Report the malaria status of this cell.
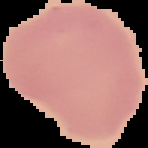

Uninfected.

image type = cell region segmented out of the field of view; surrounding area masked to black
preparation = thin blood smear
image size = 148×148 pixels